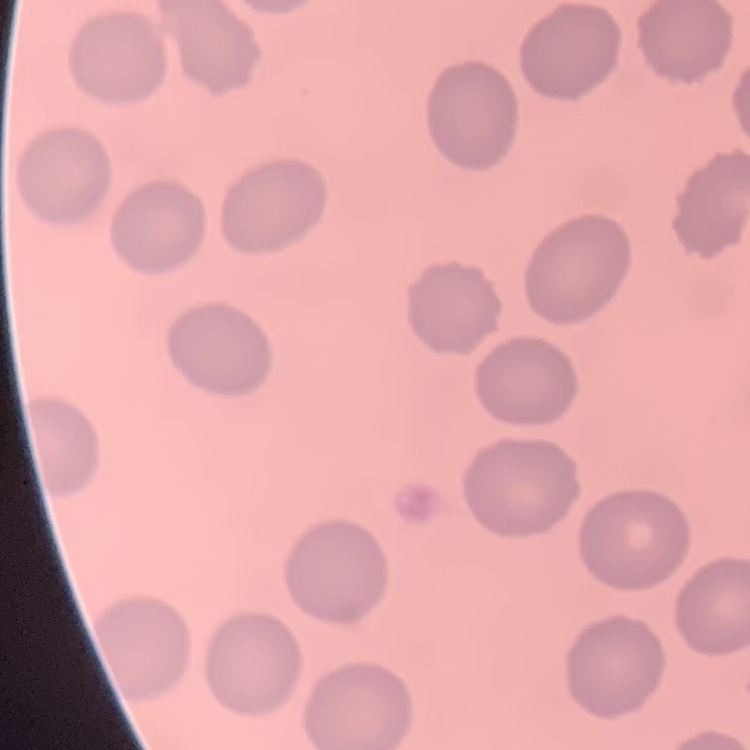

The red blood cells show no rouleaux formation. One tile cut from a larger photomicrograph. Stained with either Field's or Giemsa. Thin peripheral smear.